Report the malaria status of this cell.
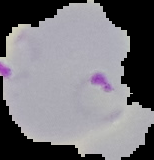
It is parasitized.

Summary:
  - Image size: 154×160 pixels
  - Image type: segmented cell region with the area outside set to black
  - Preparation: thin blood film